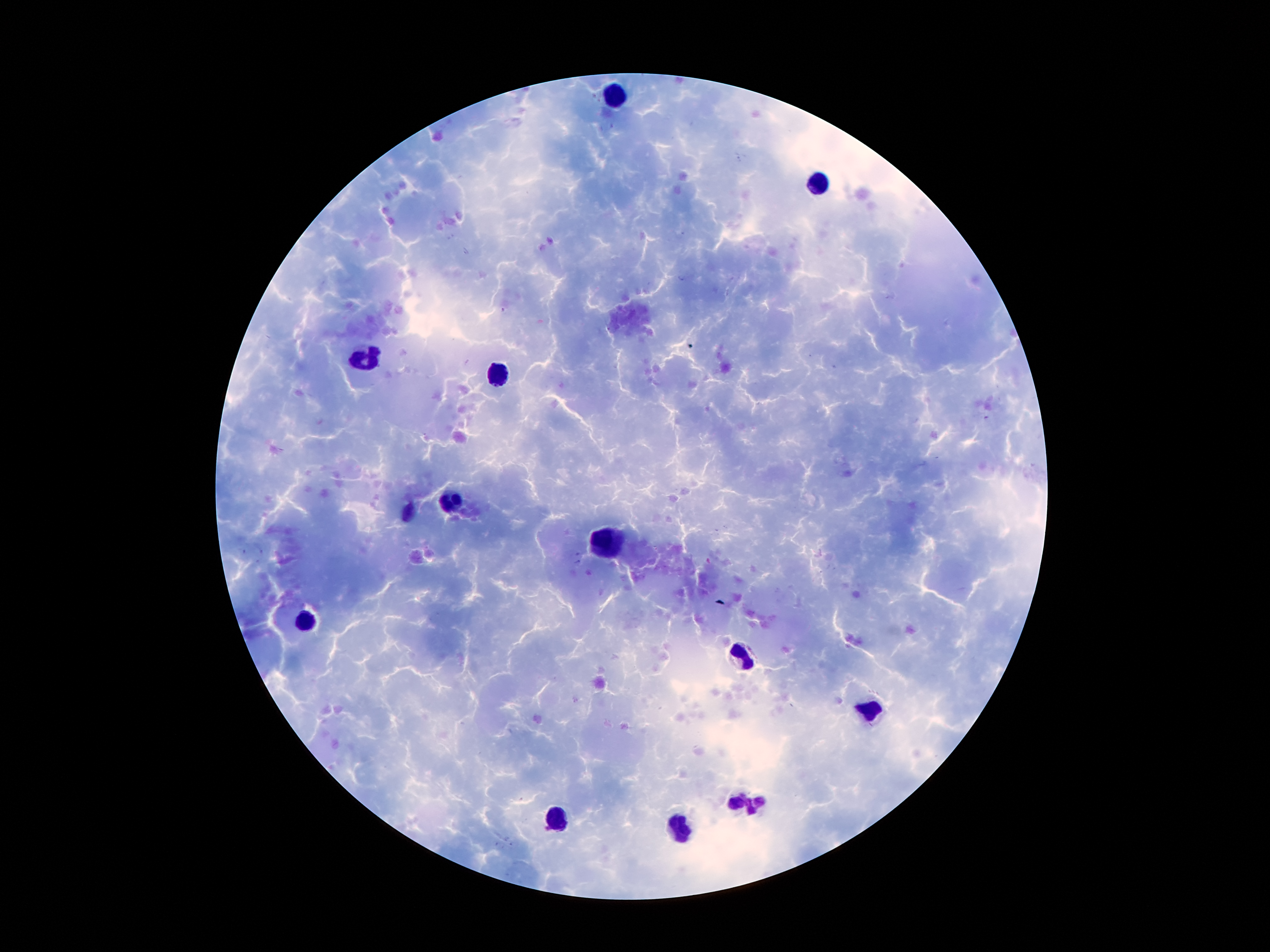
coordinate format = approximate centers as [x, y] in pixels
leukocyte locations = [613, 96], [820, 185], [366, 360], [499, 373], [450, 501], [407, 512], [607, 540], [304, 619], [745, 655], [873, 711], [747, 801], [557, 820], [679, 829]
malaria parasites = not detected
field of view = one from this slide
capture = smartphone camera through the microscope eyepiece
patient malaria status = infected with Plasmodium falciparum
preparation = thick peripheral-blood smear
magnification = 100x
image size = 1270×952 pixels
stain = Giemsa